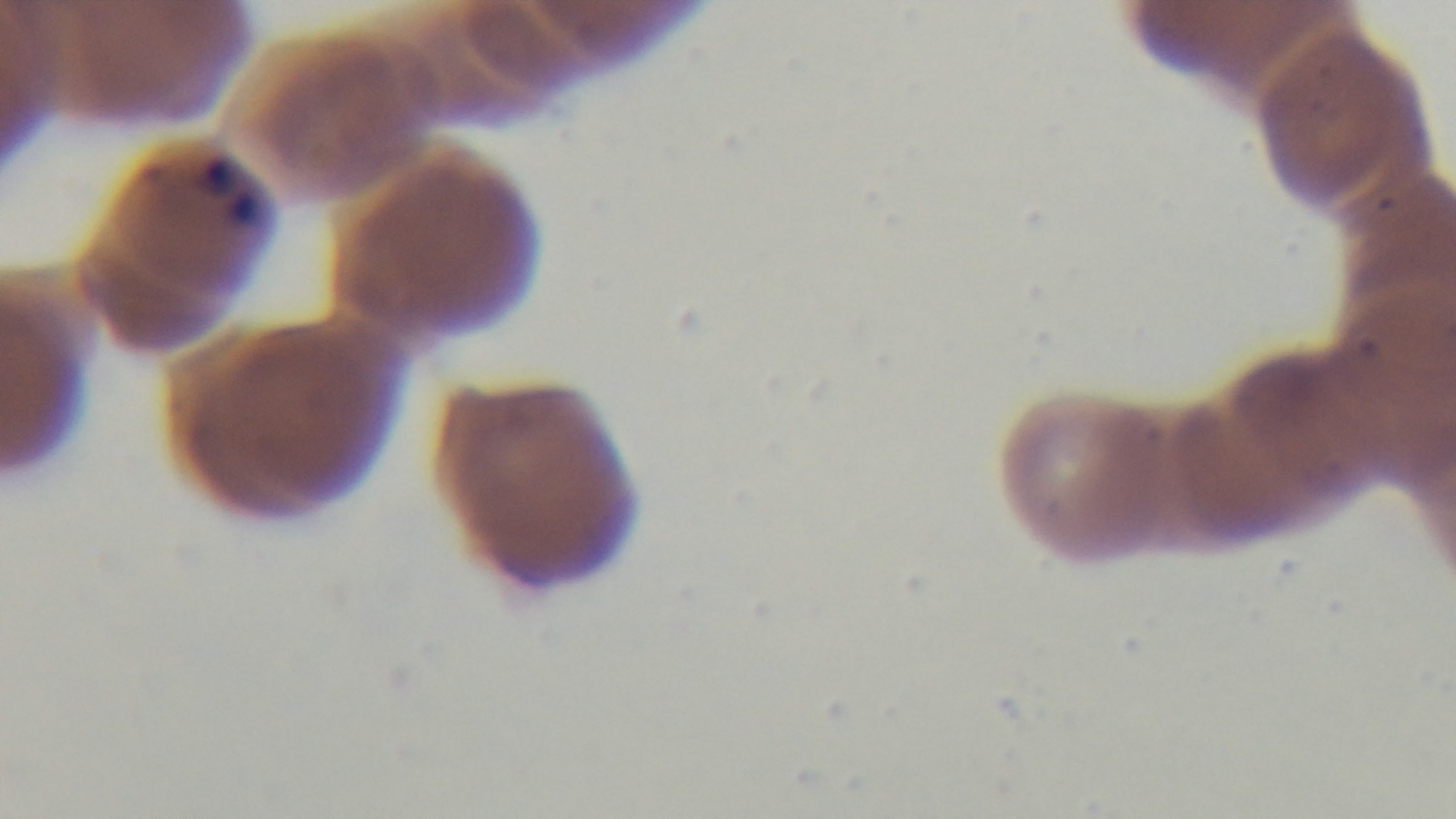
100x oil-immersion objective. Captured with a mounted 4K digital camera. Preparation: thin blood film. Malaria status: positive. Giemsa stain. One field from the slide. Light microscopy.